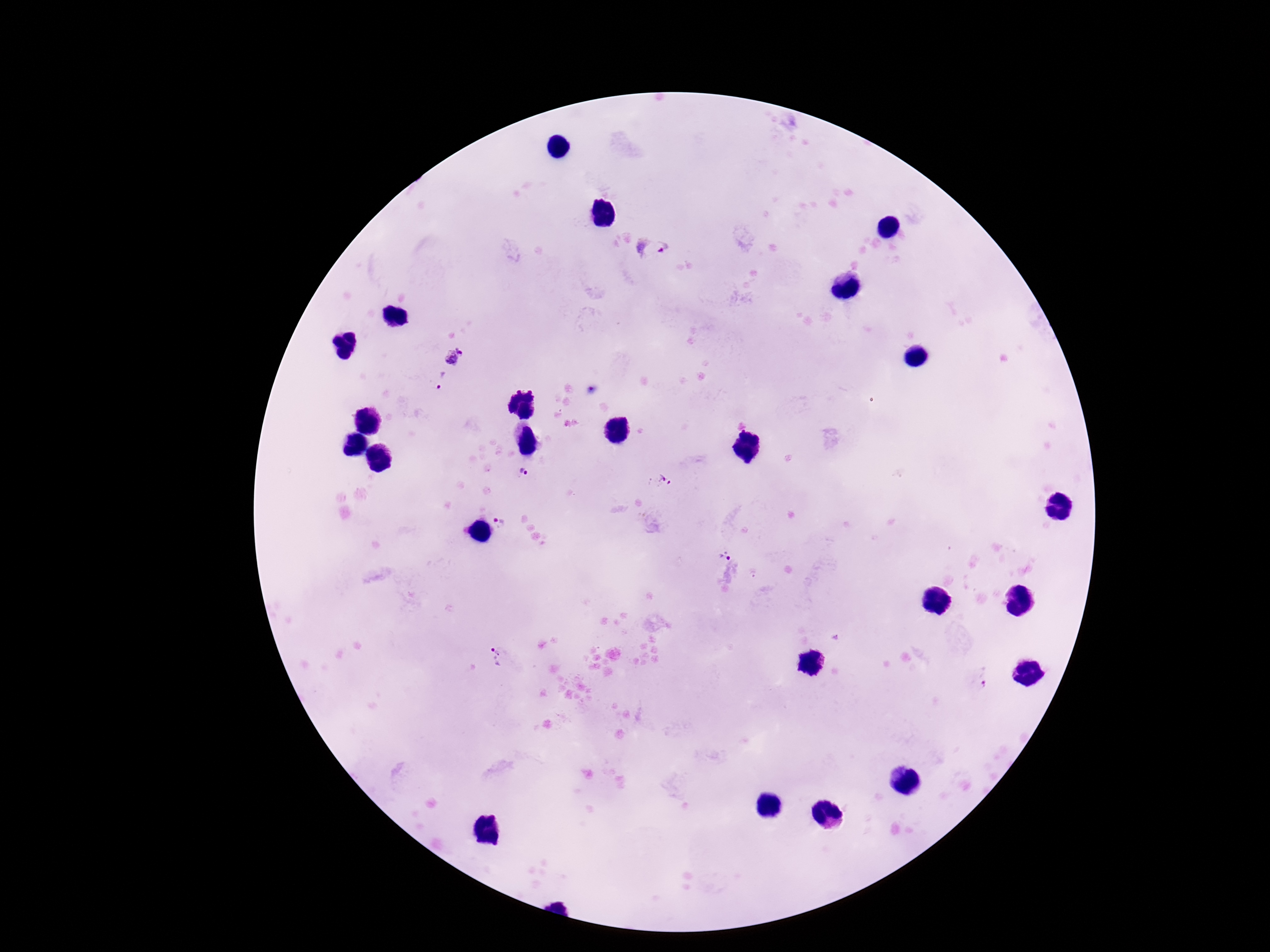

patient_malaria_status: infected
magnification: 100x
stain: Giemsa
image_size: 1270×952 pixels
plasmodium_parasite_locations: 'approximate centers as (x, y) in pixels: (652, 246), (455, 357), (440, 380), (523, 472), (666, 480), (499, 522), (724, 556), (495, 656), (981, 680)'
capture: smartphone camera through the microscope eyepiece
field_of_view: single
preparation: thick peripheral-blood smear